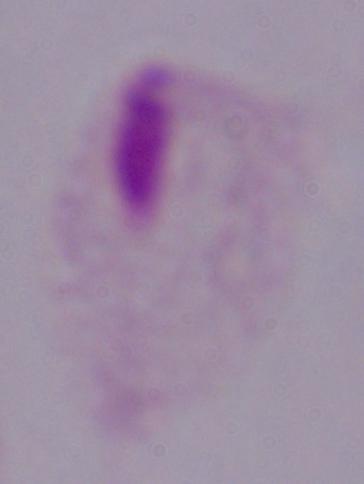
{
  "magnification": "1000x",
  "identification": "trichomonad",
  "modality": "photomicrograph"
}